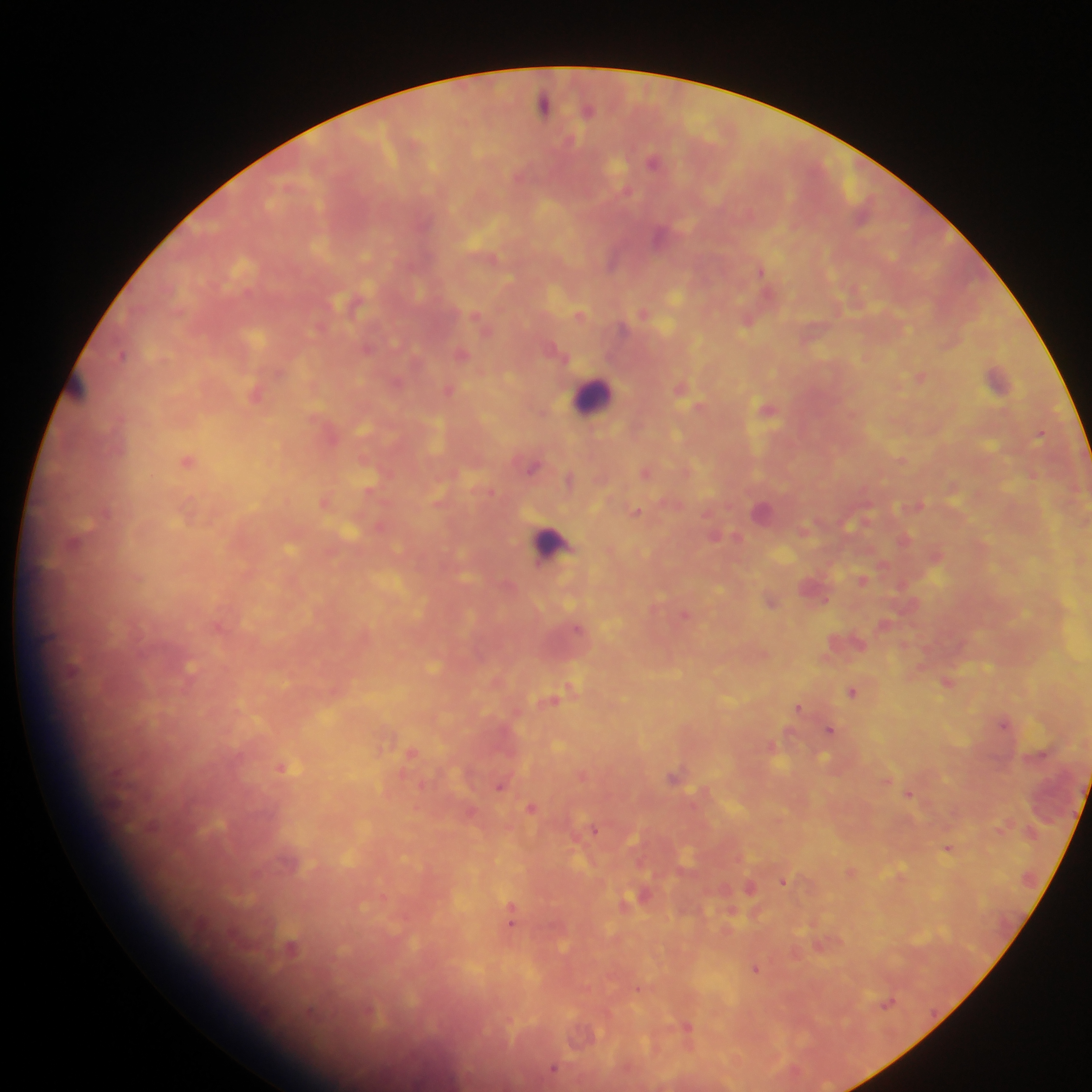 Approximate centers as x y in pixels. Malaria parasite locations: 544 105; 589 109; 653 161; 659 236; 612 262; 761 271; 368 350; 121 354; 462 354; 920 377; 998 378; 449 390; 255 395; 766 409; 1040 435; 188 461; 532 468; 646 472; 570 479; 762 511; 635 512; 862 579; 826 600; 771 601; 577 628; 947 683; 852 692; 552 700; 797 707; 1003 723; 830 729; 283 768; 675 776; 499 787; 908 794; 531 807; 593 830; 948 848; 784 881; 749 888; 510 919; 290 947; 756 969; 889 1002; 687 1027; 554 1068. Leukocyte locations: 593 395; 551 544. Collected in Ghana. Mobile-phone photograph taken through the microscope. One field of view. Image is 1092×1092 pixels. Thick blood film.